Assess for malaria.
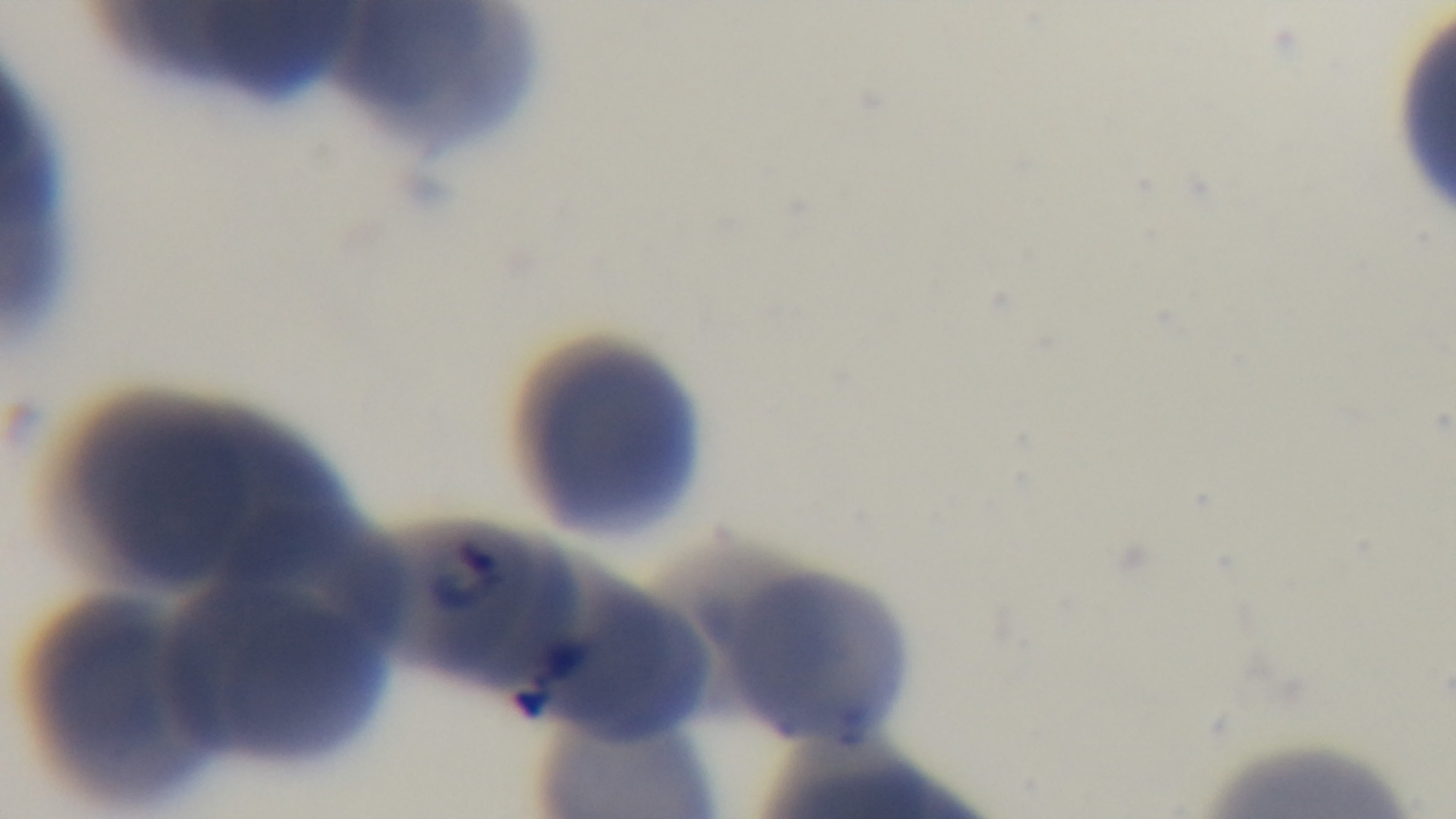

Infected.

Giemsa-stained. 100x oil-immersion objective. Preparation: thin. Single field of view. Mounted 4K digital camera. Light microscopy.